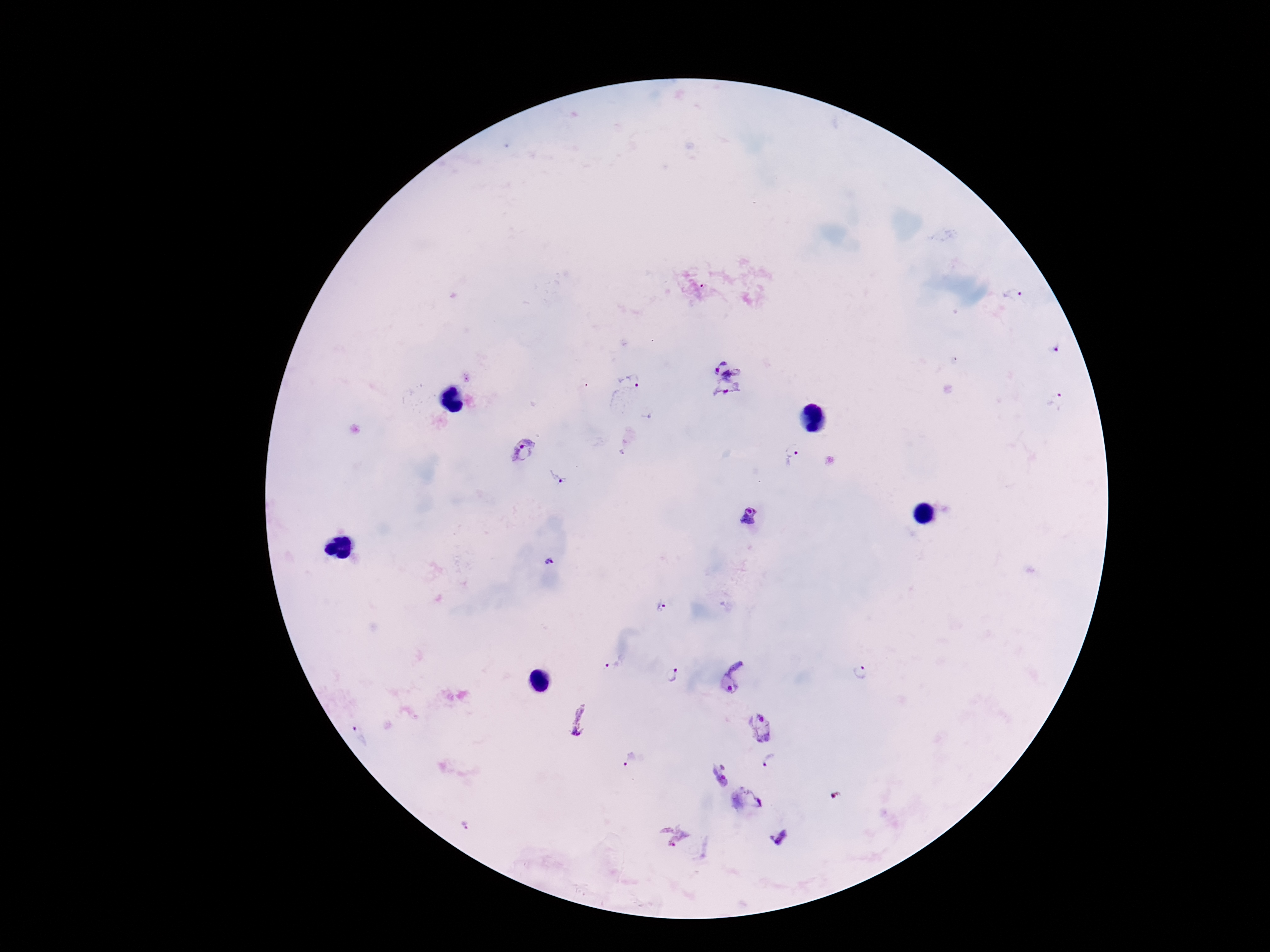
Approximate centers as (x, y) in pixels. Plasmodium parasite locations: (1014, 294), (1054, 346), (730, 350), (629, 384), (728, 399), (1057, 400), (522, 452), (792, 455), (558, 479), (749, 517), (548, 562), (662, 606), (613, 662), (860, 673), (671, 675), (738, 677), (579, 719), (758, 728), (359, 734), (631, 761), (774, 763), (748, 801), (466, 823), (672, 836), (779, 838). Image is 1270×952 pixels. Patient malaria status: infected. Smartphone photograph taken through the microscope eyepiece. Giemsa stain. 100x magnification. Thick blood smear. Single field of view.